Locate and identify every blood parasite.
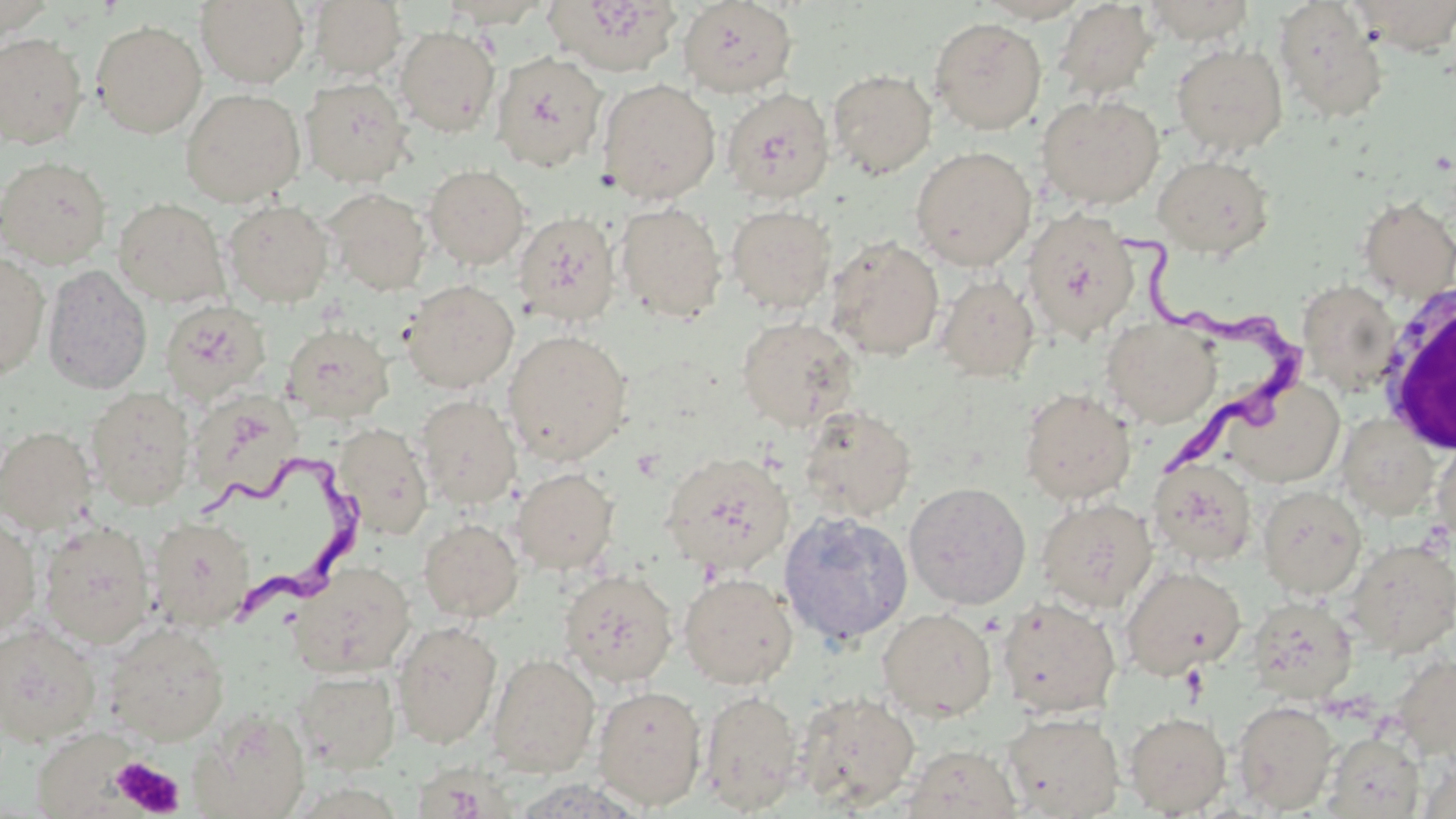

Approximate bounding boxes as [x1, y1, x2, y2] in pixels.
Trypanosoma brucei: [1115, 222, 1317, 483], [204, 447, 382, 628].
No Plasmodium falciparum, Plasmodium ovale, Plasmodium malariae, Plasmodium vivax, or Babesia divergens observed.

{
  "slide_level_diagnosis": "Trypanosoma brucei",
  "magnification": "1000x",
  "white_blood_cell_locations": "approximate bounding boxes as [x1, y1, x2, y2] in pixels: [1374, 280, 1456, 458]",
  "modality": "optical microscopy",
  "uninfected_red_blood_cell_locations": "approximate bounding boxes as [x1, y1, x2, y2] in pixels: [196, 0, 310, 88], [308, 0, 406, 81], [439, 0, 550, 28], [545, 0, 683, 77], [973, 0, 1094, 23], [1141, 0, 1256, 43], [1350, 0, 1456, 54], [677, 1, 798, 98], [1052, 1, 1159, 101], [1273, 2, 1389, 125], [0, 4, 56, 40], [929, 17, 1047, 134], [90, 20, 207, 138], [395, 26, 500, 136], [0, 32, 88, 148], [1171, 42, 1288, 157], [491, 51, 608, 172], [827, 68, 937, 179], [300, 77, 412, 188], [597, 79, 721, 204], [721, 87, 834, 204], [180, 88, 305, 206], [1035, 94, 1165, 210], [911, 146, 1036, 270], [1153, 154, 1274, 257], [0, 155, 112, 269], [424, 164, 529, 269], [324, 188, 431, 295], [1357, 195, 1456, 302], [112, 198, 231, 308], [223, 199, 334, 307], [614, 202, 727, 323], [726, 204, 836, 314], [1021, 207, 1139, 342], [512, 211, 620, 327], [826, 236, 945, 360], [0, 252, 50, 380], [41, 264, 152, 395], [935, 275, 1040, 382], [401, 279, 519, 394], [1297, 279, 1401, 394], [159, 300, 271, 406], [1101, 316, 1222, 428], [736, 317, 858, 431], [281, 323, 394, 425], [502, 329, 632, 464], [1219, 374, 1346, 488], [85, 387, 196, 511], [187, 388, 303, 505], [1019, 388, 1136, 505], [414, 395, 521, 509], [799, 405, 917, 523], [1337, 413, 1441, 521], [332, 422, 435, 540], [1, 425, 97, 535], [1433, 437, 1456, 545], [660, 451, 794, 576], [1148, 457, 1257, 566], [511, 467, 619, 575], [903, 481, 1031, 610], [1257, 485, 1367, 599], [1036, 497, 1158, 614], [778, 511, 913, 647], [0, 514, 41, 639], [148, 516, 256, 632], [418, 518, 523, 622], [37, 520, 157, 649], [1345, 538, 1456, 657], [289, 561, 415, 678], [1120, 564, 1246, 680], [560, 568, 678, 686], [678, 572, 798, 689], [1246, 596, 1358, 703], [997, 597, 1122, 718], [878, 608, 997, 722], [392, 621, 502, 749], [0, 622, 101, 746], [103, 622, 229, 745], [487, 653, 600, 777], [1390, 653, 1456, 760], [294, 669, 401, 773], [593, 685, 707, 810], [699, 689, 805, 814], [794, 690, 921, 810], [1232, 699, 1339, 814], [190, 708, 310, 819], [1123, 710, 1232, 816], [1001, 711, 1124, 818], [35, 727, 147, 816], [1324, 731, 1425, 818], [900, 744, 1023, 819], [410, 765, 508, 819]",
  "platelet_locations": "approximate bounding boxes as [x1, y1, x2, y2] in pixels: [111, 756, 184, 816]",
  "preparation": "thin blood smear",
  "field_of_view": "one of a larger specimen",
  "image_size": "1456×819 pixels",
  "stain": "May-Grünwald-Giemsa"
}